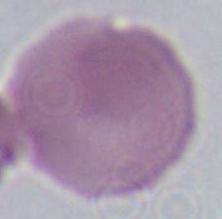

Summary:
  - Identification: red blood cell
  - Modality: micrograph
  - Magnification: 1000x